Identify the parasite.
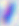
Toxoplasma gondii.

400x magnification. Micrograph.